Assess this cell for malaria.
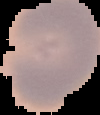
Uninfected.

Summary:
  - Image size: 100×115 pixels
  - Preparation: thin blood smear
  - Image type: segmented cell region on a black background